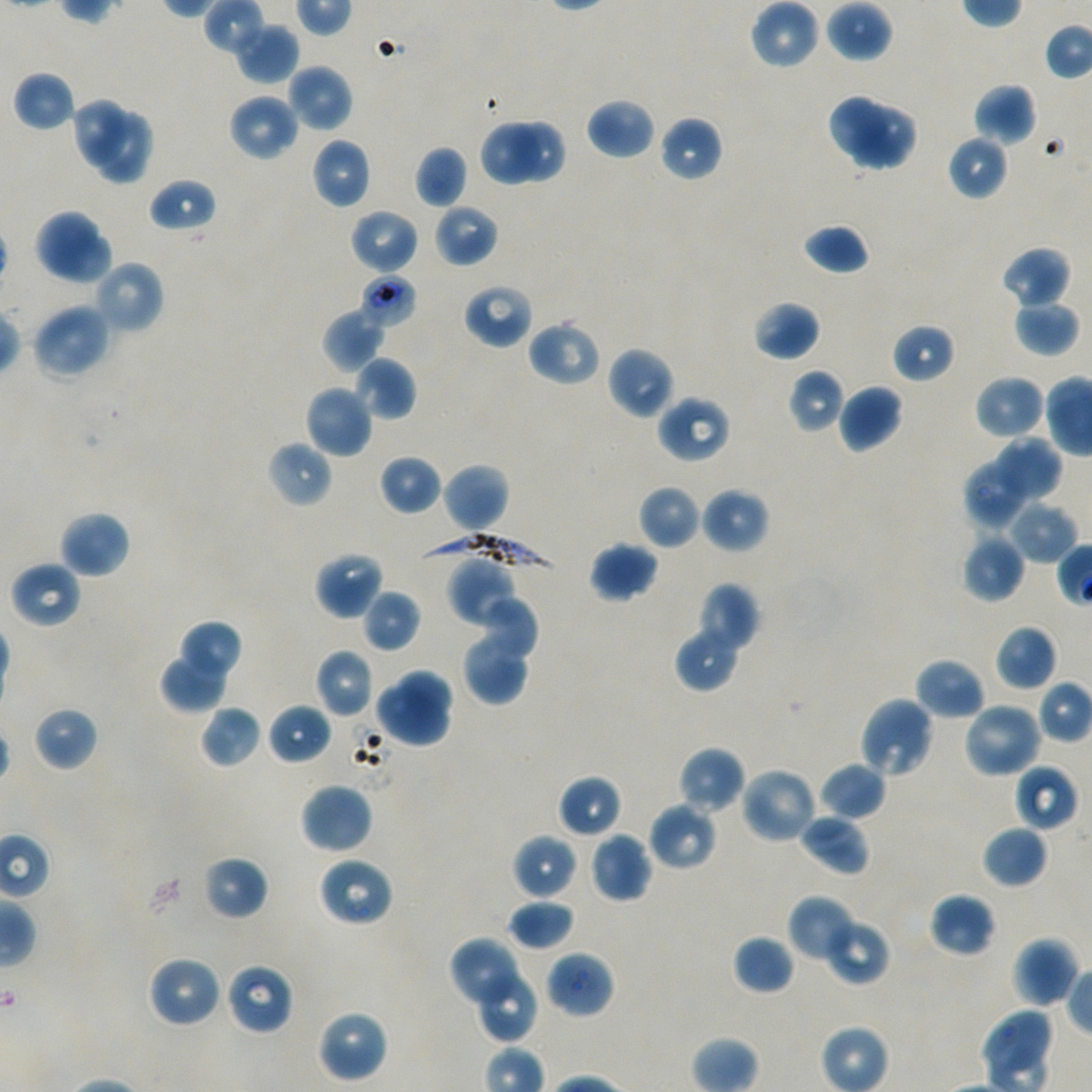
Not every red blood cell is marked. A life-cycle stage — or a range of stages, where the recorded stages span more than one — follows each staged infected red blood cell.
image size = 1092×1092 pixels
locations of infected red blood cells = approximate bounding rectangles given as corner coordinates in pixels from the top-left: (x1=358, y1=274, x2=418, y2=329) trophozoite; (x1=416, y1=532, x2=557, y2=570)
culture = P. falciparum strain NF54, static, in vitro
preparation = thin blood smear
donor blood group = A+/O+
field of view = single
locations of uninfected red blood cells = approximate bounding rectangles given as corner coordinates in pixels from the top-left: (x1=750, y1=0, x2=819, y2=69), (x1=826, y1=0, x2=894, y2=62), (x1=234, y1=22, x2=299, y2=85), (x1=286, y1=64, x2=354, y2=133), (x1=13, y1=70, x2=76, y2=132), (x1=972, y1=83, x2=1037, y2=145), (x1=826, y1=92, x2=891, y2=156), (x1=228, y1=93, x2=299, y2=162), (x1=70, y1=98, x2=132, y2=170), (x1=586, y1=98, x2=655, y2=160), (x1=850, y1=102, x2=917, y2=172), (x1=95, y1=109, x2=154, y2=185), (x1=659, y1=115, x2=723, y2=182), (x1=478, y1=117, x2=541, y2=187), (x1=509, y1=120, x2=568, y2=184), (x1=947, y1=134, x2=1008, y2=202), (x1=310, y1=137, x2=371, y2=209), (x1=414, y1=146, x2=467, y2=209), (x1=149, y1=177, x2=217, y2=234), (x1=433, y1=202, x2=499, y2=268), (x1=33, y1=208, x2=99, y2=276), (x1=349, y1=208, x2=420, y2=274), (x1=802, y1=223, x2=871, y2=276), (x1=51, y1=232, x2=114, y2=286), (x1=1000, y1=246, x2=1072, y2=310), (x1=93, y1=259, x2=165, y2=336), (x1=462, y1=284, x2=533, y2=349), (x1=1013, y1=299, x2=1080, y2=357), (x1=752, y1=300, x2=820, y2=361), (x1=32, y1=303, x2=113, y2=381), (x1=322, y1=308, x2=385, y2=373), (x1=527, y1=320, x2=601, y2=386), (x1=892, y1=323, x2=956, y2=383), (x1=606, y1=346, x2=676, y2=420), (x1=354, y1=357, x2=416, y2=421), (x1=788, y1=368, x2=846, y2=433), (x1=973, y1=374, x2=1045, y2=441), (x1=304, y1=384, x2=374, y2=458), (x1=837, y1=384, x2=903, y2=453), (x1=656, y1=394, x2=732, y2=464), (x1=996, y1=433, x2=1062, y2=506), (x1=266, y1=439, x2=333, y2=509), (x1=378, y1=454, x2=443, y2=515), (x1=962, y1=459, x2=1025, y2=531), (x1=442, y1=462, x2=510, y2=534), (x1=638, y1=484, x2=702, y2=549), (x1=700, y1=488, x2=769, y2=553), (x1=1006, y1=501, x2=1078, y2=564), (x1=58, y1=510, x2=131, y2=579), (x1=961, y1=533, x2=1026, y2=603), (x1=588, y1=541, x2=659, y2=603), (x1=314, y1=550, x2=385, y2=620), (x1=445, y1=554, x2=521, y2=629), (x1=10, y1=560, x2=82, y2=629), (x1=696, y1=583, x2=761, y2=655), (x1=361, y1=588, x2=420, y2=653), (x1=479, y1=592, x2=540, y2=659), (x1=460, y1=616, x2=534, y2=706), (x1=177, y1=619, x2=243, y2=685), (x1=674, y1=624, x2=742, y2=692), (x1=994, y1=624, x2=1057, y2=691), (x1=159, y1=647, x2=231, y2=713), (x1=314, y1=649, x2=374, y2=718), (x1=915, y1=657, x2=985, y2=721), (x1=395, y1=666, x2=455, y2=727), (x1=374, y1=682, x2=455, y2=749), (x1=858, y1=695, x2=936, y2=780), (x1=961, y1=701, x2=1043, y2=779), (x1=268, y1=702, x2=333, y2=765), (x1=199, y1=705, x2=263, y2=769), (x1=33, y1=706, x2=98, y2=771), (x1=677, y1=746, x2=746, y2=814), (x1=818, y1=761, x2=886, y2=821), (x1=1013, y1=763, x2=1078, y2=833), (x1=740, y1=765, x2=818, y2=845), (x1=557, y1=774, x2=622, y2=838), (x1=299, y1=782, x2=374, y2=854), (x1=647, y1=801, x2=718, y2=871), (x1=797, y1=812, x2=870, y2=876), (x1=981, y1=824, x2=1049, y2=889), (x1=511, y1=833, x2=577, y2=900), (x1=589, y1=833, x2=653, y2=904), (x1=202, y1=855, x2=269, y2=920), (x1=318, y1=856, x2=394, y2=927), (x1=928, y1=892, x2=996, y2=958), (x1=786, y1=894, x2=856, y2=963), (x1=507, y1=898, x2=575, y2=951), (x1=823, y1=917, x2=891, y2=987), (x1=732, y1=934, x2=795, y2=995), (x1=448, y1=935, x2=523, y2=1011), (x1=1011, y1=936, x2=1080, y2=1008), (x1=545, y1=949, x2=615, y2=1019), (x1=147, y1=954, x2=223, y2=1029), (x1=225, y1=962, x2=294, y2=1036), (x1=471, y1=967, x2=538, y2=1042), (x1=981, y1=1005, x2=1053, y2=1073), (x1=316, y1=1008, x2=388, y2=1082)
objective = 100x, oil immersion, numerical aperture 1.45
stain = Giemsa